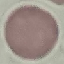

Summary:
  - Malaria status: uninfected
  - Preparation: thin smear
  - Image type: cell patch, automatically extracted from a larger field of view and resized to 64 × 64 pixels
  - Stain: Giemsa
  - Capture: smartphone through the microscope eyepiece